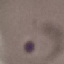 Malaria status: parasitized. Automatically extracted cell patch, resized to 64 × 64 pixels. Giemsa-stained preparation. Acquired by smartphone through the microscope eyepiece. Thin blood film.